State which parasite is depicted.
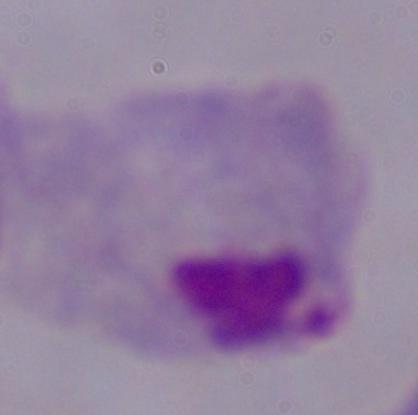
A trichomonad.

modality = photomicrograph
magnification = 1000x